Outline platelets.
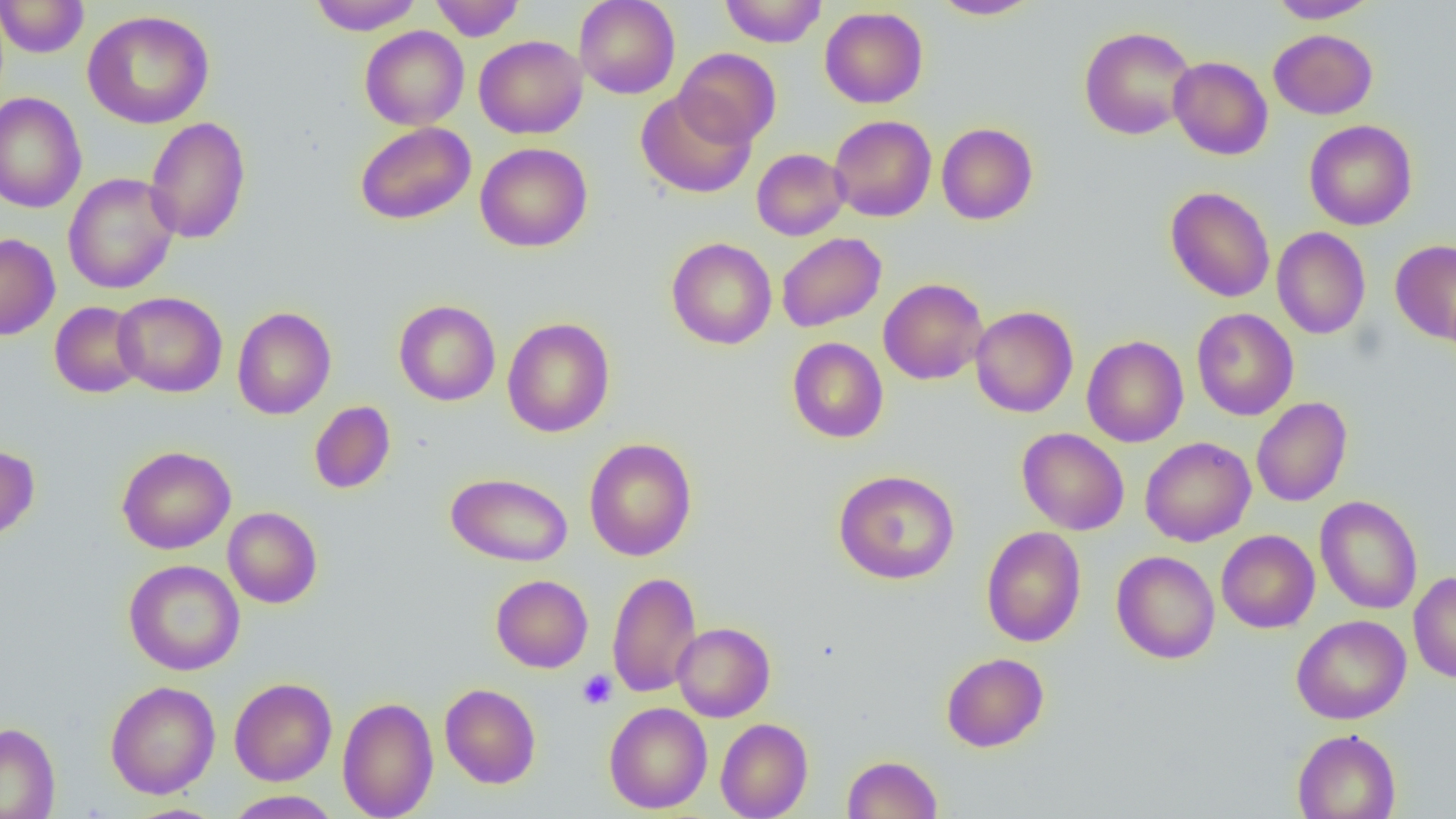

Approximate bounding boxes as (x1,y1)-(x2,y2) corner pairs in pixels.
Platelets: (577,670)-(617,709).

Summary:
  - Uninfected red blood cell locations: (0,0)-(89,58), (307,0)-(424,34), (430,0)-(525,41), (574,0)-(681,99), (719,0)-(827,47), (930,0)-(1043,19), (1269,0)-(1379,23), (819,6)-(928,108), (82,10)-(215,129), (360,25)-(469,130), (1079,25)-(1197,140), (1269,29)-(1377,119), (474,35)-(588,139), (674,48)-(781,148), (1169,56)-(1272,160), (635,89)-(756,198), (0,92)-(86,213), (829,115)-(937,222), (144,116)-(251,245), (1304,120)-(1417,230), (355,121)-(476,225), (936,122)-(1038,225), (475,142)-(592,252), (751,148)-(849,240), (63,173)-(179,295), (1165,186)-(1275,302), (1272,227)-(1371,339), (776,232)-(886,332), (0,233)-(60,341), (666,237)-(777,350), (1390,239)-(1456,343), (878,278)-(988,385), (113,291)-(227,397), (393,299)-(501,406), (49,301)-(146,398), (969,305)-(1078,418), (232,306)-(336,419), (1192,308)-(1299,421), (502,317)-(615,438), (1082,335)-(1188,447), (787,337)-(888,443), (1251,397)-(1352,507), (309,401)-(396,494), (1017,428)-(1129,535), (1140,436)-(1256,546), (584,437)-(697,561), (0,443)-(40,543), (116,445)-(236,554), (833,468)-(960,585), (445,472)-(573,567), (1315,495)-(1422,614), (222,506)-(323,608), (981,526)-(1086,647), (1216,529)-(1320,633), (1111,550)-(1220,664), (123,559)-(245,675), (607,571)-(702,698), (1408,571)-(1456,683), (491,574)-(593,673), (1291,614)-(1411,724), (672,622)-(775,721), (941,652)-(1049,752), (229,677)-(337,785), (105,680)-(221,799), (440,683)-(541,788), (337,696)-(438,818), (603,702)-(712,813), (715,718)-(813,819), (0,722)-(60,818), (1293,729)-(1400,818), (842,755)-(943,818), (224,790)-(342,819)
  - Slide-level diagnosis: no evidence of blood parasites
  - Preparation: thin blood smear
  - Magnification: 1000x
  - Field of view: single
  - Image size: 1456×819 pixels
  - Modality: optical microscopy